Describe the morphology of the red blood cells.
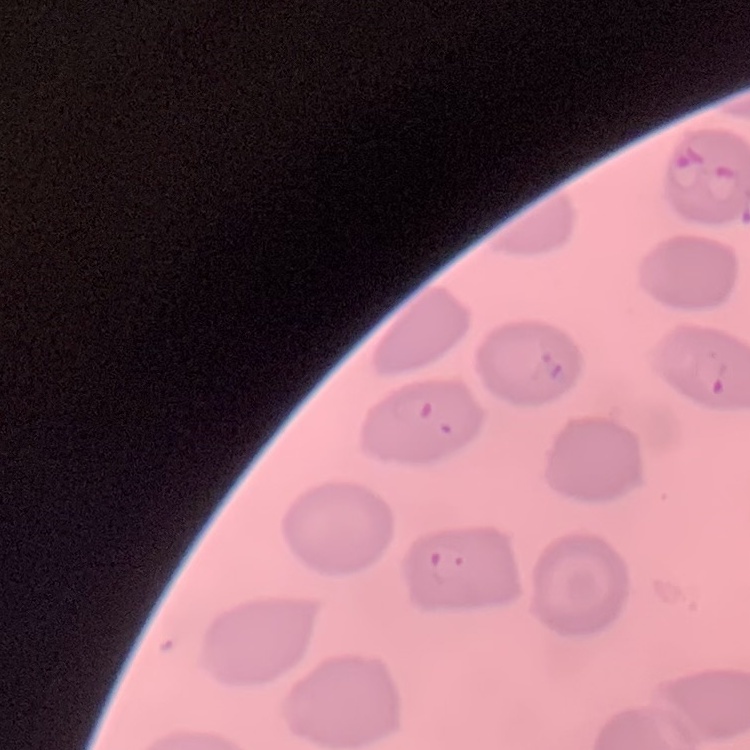
No rouleaux formation.

image type = one tile cut from a larger photomicrograph
stain = Field's or Giemsa
preparation = thin blood film